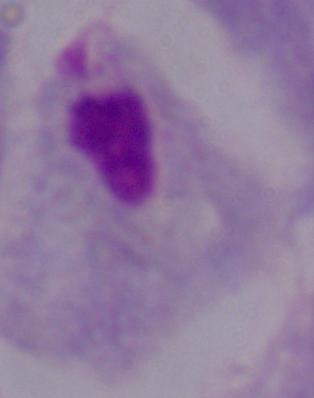
{
  "magnification": "1000x",
  "identification": "trichomonad",
  "modality": "micrograph"
}